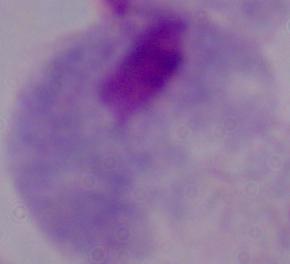
magnification = 1000x
modality = photomicrograph
identification = trichomonad